Report the malaria status of this cell.
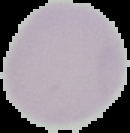

It is uninfected.

preparation = thin blood smear
image size = 130×133 pixels
image type = cell region segmented out of the field of view; surrounding area masked to black